Assess this cell for malaria.
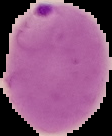

It is parasitized.

image type = segmented cell region with the area outside set to black
preparation = thin blood film
image size = 112×136 pixels